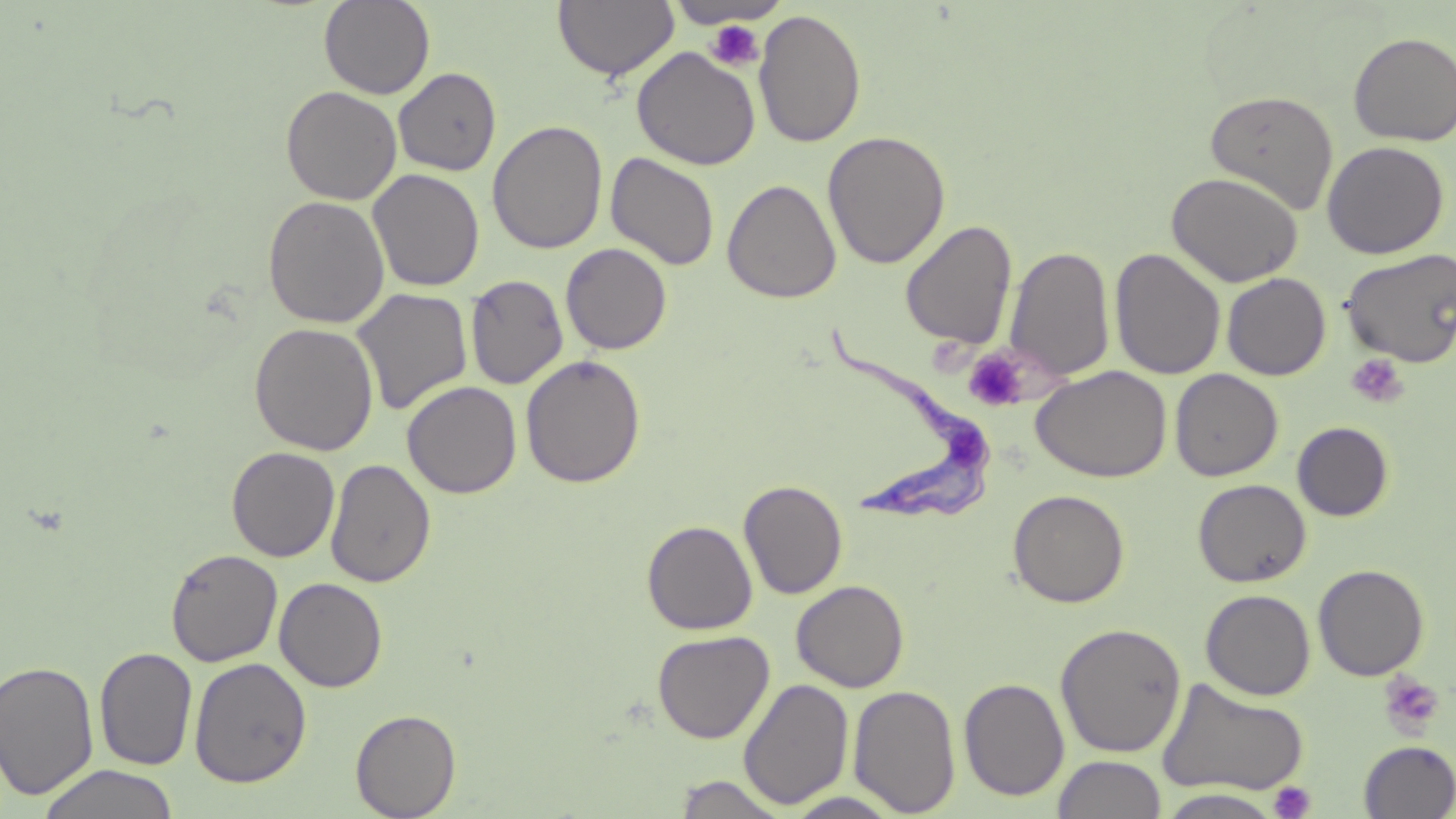

slide-level diagnosis = Trypanosoma brucei
image size = 1456×819 pixels
modality = optical microscopy
uninfected red blood cell locations = approximate bounding boxes as named x1/y1/x2/y2 corners in pixels: (x1=319, y1=0, x2=435, y2=100), (x1=552, y1=1, x2=680, y2=82), (x1=667, y1=1, x2=790, y2=29), (x1=753, y1=8, x2=867, y2=148), (x1=1348, y1=31, x2=1456, y2=146), (x1=631, y1=47, x2=761, y2=170), (x1=394, y1=68, x2=501, y2=176), (x1=281, y1=86, x2=402, y2=205), (x1=1204, y1=90, x2=1338, y2=214), (x1=487, y1=120, x2=607, y2=254), (x1=822, y1=130, x2=951, y2=269), (x1=1322, y1=140, x2=1449, y2=259), (x1=605, y1=151, x2=720, y2=271), (x1=368, y1=169, x2=485, y2=291), (x1=1166, y1=172, x2=1304, y2=287), (x1=722, y1=179, x2=841, y2=303), (x1=262, y1=195, x2=390, y2=328), (x1=900, y1=219, x2=1018, y2=350), (x1=561, y1=242, x2=672, y2=355), (x1=1005, y1=245, x2=1115, y2=383), (x1=1110, y1=248, x2=1225, y2=380), (x1=1341, y1=248, x2=1456, y2=367), (x1=1222, y1=272, x2=1331, y2=380), (x1=465, y1=274, x2=568, y2=390), (x1=351, y1=288, x2=472, y2=415), (x1=249, y1=322, x2=379, y2=455), (x1=521, y1=355, x2=646, y2=488), (x1=1031, y1=365, x2=1171, y2=482), (x1=1170, y1=369, x2=1283, y2=481), (x1=402, y1=380, x2=522, y2=499), (x1=1292, y1=421, x2=1394, y2=521), (x1=226, y1=446, x2=340, y2=562), (x1=325, y1=458, x2=436, y2=588), (x1=738, y1=479, x2=848, y2=600), (x1=1193, y1=479, x2=1311, y2=587), (x1=1008, y1=489, x2=1130, y2=608), (x1=642, y1=520, x2=758, y2=635), (x1=178, y1=547, x2=295, y2=784), (x1=165, y1=548, x2=283, y2=667), (x1=1313, y1=564, x2=1429, y2=681), (x1=274, y1=577, x2=388, y2=693), (x1=791, y1=580, x2=909, y2=692), (x1=1200, y1=588, x2=1316, y2=700), (x1=1055, y1=622, x2=1187, y2=757), (x1=652, y1=629, x2=774, y2=743), (x1=94, y1=647, x2=198, y2=770), (x1=189, y1=657, x2=312, y2=788), (x1=0, y1=659, x2=99, y2=799), (x1=959, y1=677, x2=1069, y2=801), (x1=1157, y1=677, x2=1310, y2=797), (x1=739, y1=678, x2=854, y2=809), (x1=848, y1=684, x2=962, y2=816), (x1=350, y1=709, x2=461, y2=818), (x1=1359, y1=740, x2=1456, y2=818), (x1=1051, y1=755, x2=1167, y2=819), (x1=37, y1=763, x2=178, y2=819), (x1=671, y1=774, x2=790, y2=818), (x1=1156, y1=789, x2=1285, y2=818), (x1=784, y1=791, x2=904, y2=818)
stain = May-Grünwald-Giemsa
magnification = 1000x
platelet locations = approximate bounding boxes as named x1/y1/x2/y2 corners in pixels: (x1=703, y1=18, x2=765, y2=72), (x1=963, y1=347, x2=1035, y2=412), (x1=1346, y1=354, x2=1410, y2=408), (x1=1377, y1=669, x2=1445, y2=739), (x1=1268, y1=781, x2=1316, y2=818)
field of view = single
preparation = thin blood smear
Trypanosoma brucei locations = approximate bounding boxes as named x1/y1/x2/y2 corners in pixels: (x1=822, y1=326, x2=994, y2=523)